Give the extent of all uninfected red blood cells.
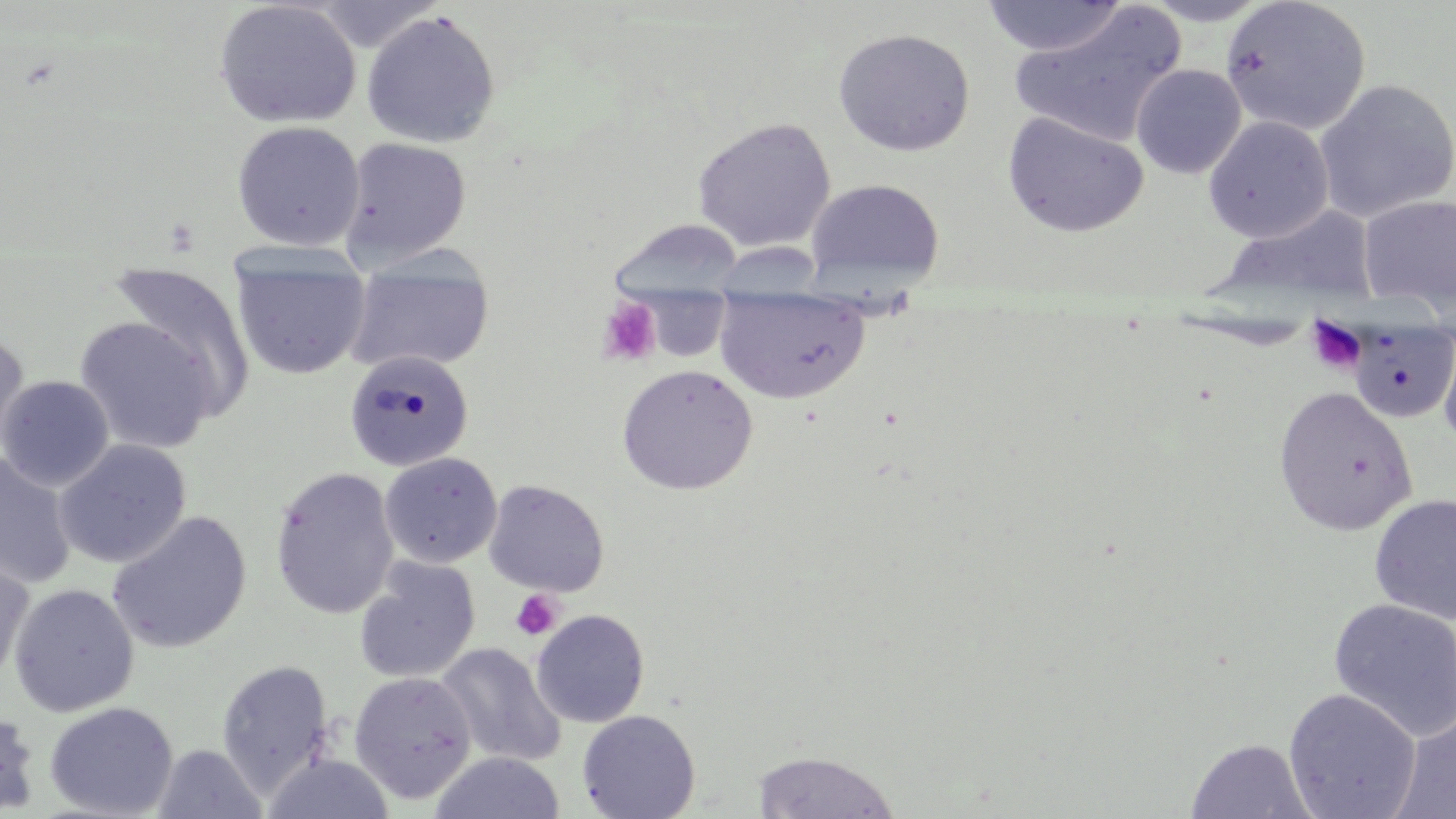
Approximate bounding boxes as [x1, y1, x2, y2] in pixels.
Uninfected red blood cells: [213, 0, 362, 129], [981, 0, 1130, 57], [1138, 0, 1275, 26], [1008, 1, 1187, 149], [1220, 1, 1371, 136], [361, 10, 501, 149], [833, 28, 975, 157], [1131, 63, 1247, 179], [1314, 78, 1456, 222], [1002, 111, 1149, 238], [1203, 116, 1334, 243], [692, 117, 836, 252], [231, 120, 365, 251], [339, 136, 472, 268], [805, 178, 945, 291], [1359, 194, 1456, 312], [1217, 205, 1378, 306], [610, 219, 745, 303], [230, 248, 372, 381], [344, 248, 495, 375], [106, 260, 256, 415], [714, 287, 871, 404], [73, 317, 218, 455], [1346, 318, 1456, 423], [1437, 323, 1456, 453], [0, 334, 31, 459], [344, 350, 474, 472], [616, 365, 758, 495], [0, 375, 114, 490], [1273, 386, 1418, 537], [53, 440, 191, 569], [0, 451, 77, 590], [379, 453, 502, 568], [270, 467, 400, 620], [483, 479, 609, 597], [1368, 493, 1456, 625], [107, 510, 252, 654], [0, 547, 35, 689], [353, 557, 480, 684], [8, 583, 139, 717], [1327, 598, 1456, 743], [531, 609, 650, 728], [435, 642, 566, 767], [217, 660, 334, 795], [348, 671, 477, 804], [1283, 688, 1421, 819], [44, 702, 179, 818], [0, 706, 40, 815], [1390, 706, 1456, 818], [577, 709, 701, 819], [1186, 738, 1317, 819], [152, 743, 267, 819], [752, 750, 901, 818], [429, 752, 566, 818], [261, 753, 397, 818].

slide-level diagnosis = no evidence of blood parasites
platelet locations = approximate bounding boxes as [x1, y1, x2, y2] in pixels: [597, 297, 661, 367], [1304, 315, 1367, 375], [510, 589, 564, 641]
stain = May-Grünwald-Giemsa
modality = light microscopy
magnification = 1000x
preparation = thin blood film
image size = 1456×819 pixels
field of view = one of a larger specimen